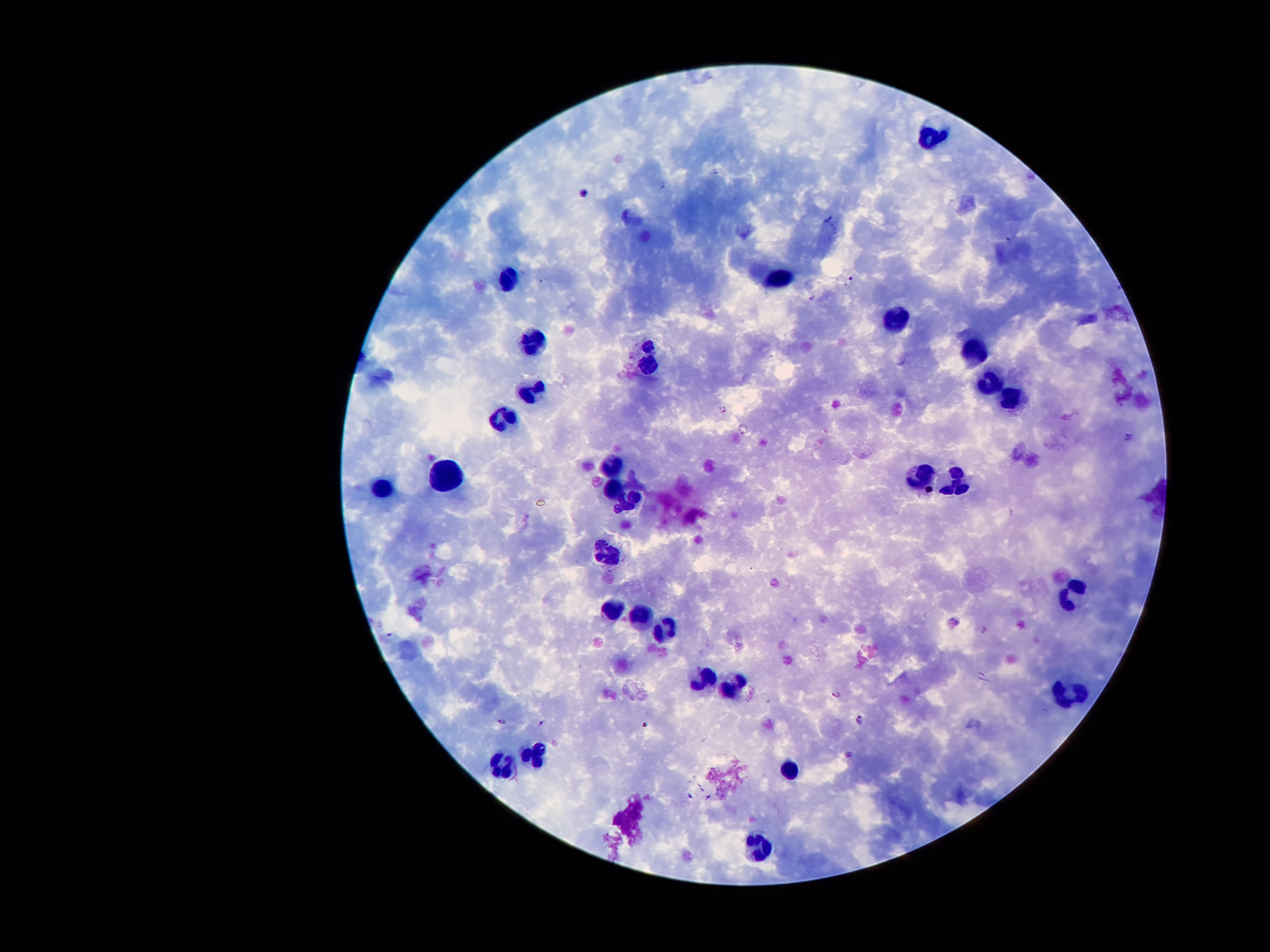
coordinate format = approximate centers as [x, y] in pixels
leukocyte locations = [930, 135], [779, 278], [506, 279], [893, 320], [536, 343], [973, 350], [648, 366], [987, 383], [534, 390], [1009, 400], [506, 420], [610, 467], [443, 474], [923, 477], [957, 482], [384, 488], [613, 490], [629, 504], [606, 556], [1072, 595], [611, 611], [642, 614], [664, 628], [702, 679], [732, 690], [1067, 695], [532, 756], [502, 765], [789, 768], [758, 851]
malaria parasite locations = [716, 170], [662, 185], [583, 193], [829, 219], [1008, 239], [852, 280], [541, 281], [813, 294], [647, 346], [722, 409], [744, 430], [1128, 437], [955, 621], [837, 695], [858, 720], [502, 721], [541, 722], [647, 726], [848, 754]
patient malaria status = infected with Plasmodium falciparum
image size = 1270×952 pixels
preparation = thick peripheral-blood smear
field of view = one from this slide
magnification = 100x
capture = smartphone camera through the microscope eyepiece
stain = Giemsa